Comment on the morphology of the red blood cells.
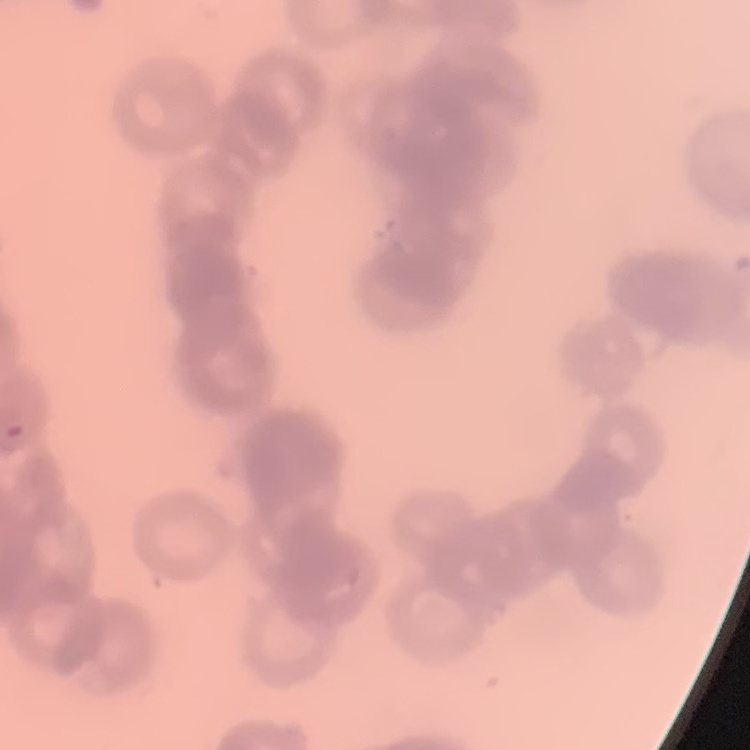

They show rouleaux formation.

preparation = thin blood smear
image type = one tile cut from a larger photomicrograph
stain = Field's or Giemsa